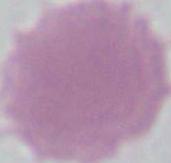

magnification = 1000x
identification = erythrocyte
modality = photomicrograph